Locate every Plasmodium parasite.
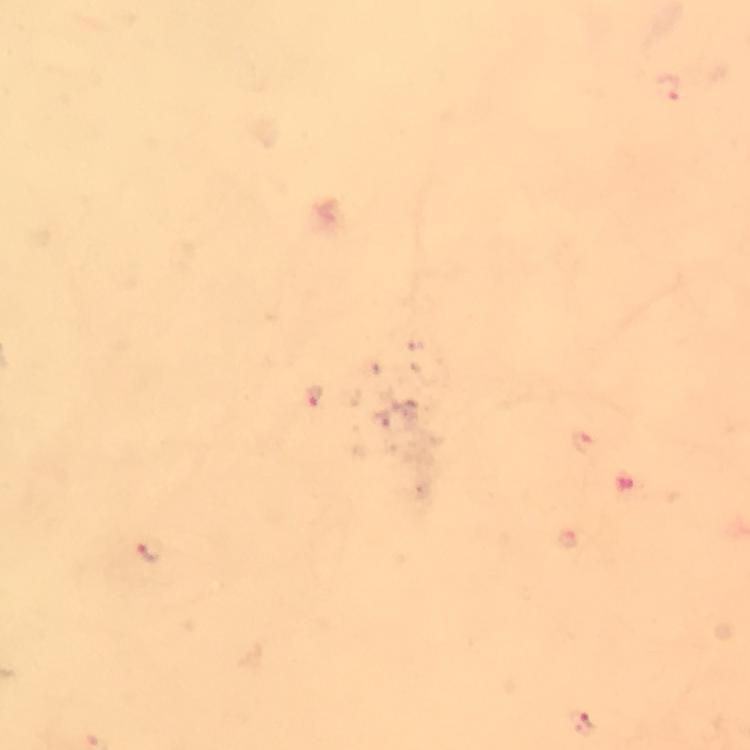

Approximate object centers, in pixels from the top-left corner.
Plasmodium parasites: (x=669, y=88), (x=312, y=395), (x=151, y=553), (x=581, y=724).

context = from a diagnostic examination for malaria
immersion oil = applied
image size = 750×750 pixels
stain = Giemsa
magnification = 100x
cropped from = one field of view
capture = smartphone mounted on the microscope
preparation = thick smear